Classify this cell by malaria status.
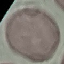

It is uninfected.

Cell patch, automatically extracted from a larger field of view and resized to 64 × 64 pixels. Acquired by smartphone through the microscope eyepiece. Giemsa-stained preparation. Thin blood film.